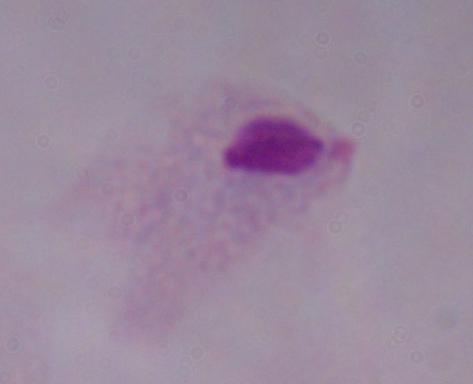
{
  "modality": "photomicrograph",
  "magnification": "1000x",
  "identification": "trichomonad"
}